Classify this cell by malaria status.
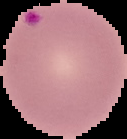

Parasitized.

From a thin blood smear. Image is 127×139 pixels. Segmented cell region on a black background.